Report the malaria status of this cell.
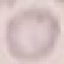

It is uninfected.

Summary:
  - Preparation: thin blood smear
  - Stain: Giemsa
  - Capture: smartphone through the microscope eyepiece
  - Image type: cell patch, automatically extracted from a larger field of view and resized to 64 × 64 pixels